State which parasite is depicted.
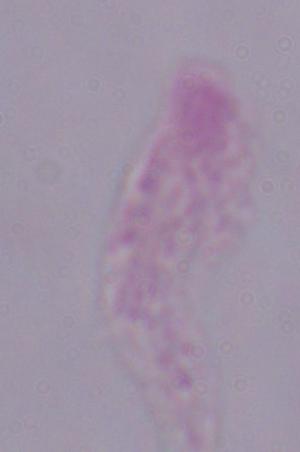

A trichomonad.

magnification = 1000x
modality = micrograph